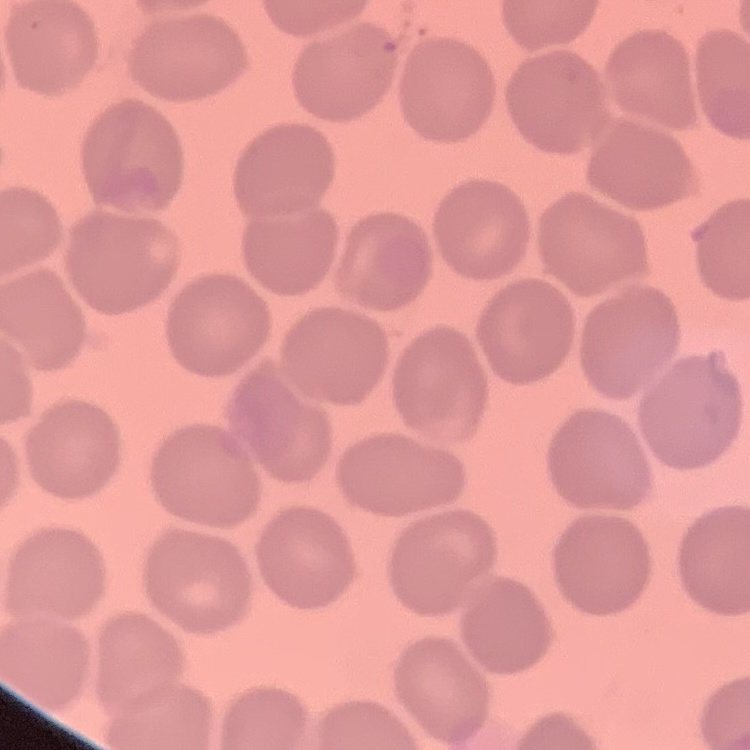

The red blood cells exhibit no rouleaux formation. Square crop of a larger photomicrograph. Thin blood smear. Stained with either Field's or Giemsa.